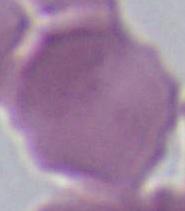
identification = erythrocyte
modality = photomicrograph
magnification = 1000x